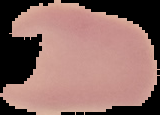 Cell region segmented out of the field of view; the surrounding area is masked to black. Malaria status: uninfected. Image is 160×115 pixels. From a thin blood film.